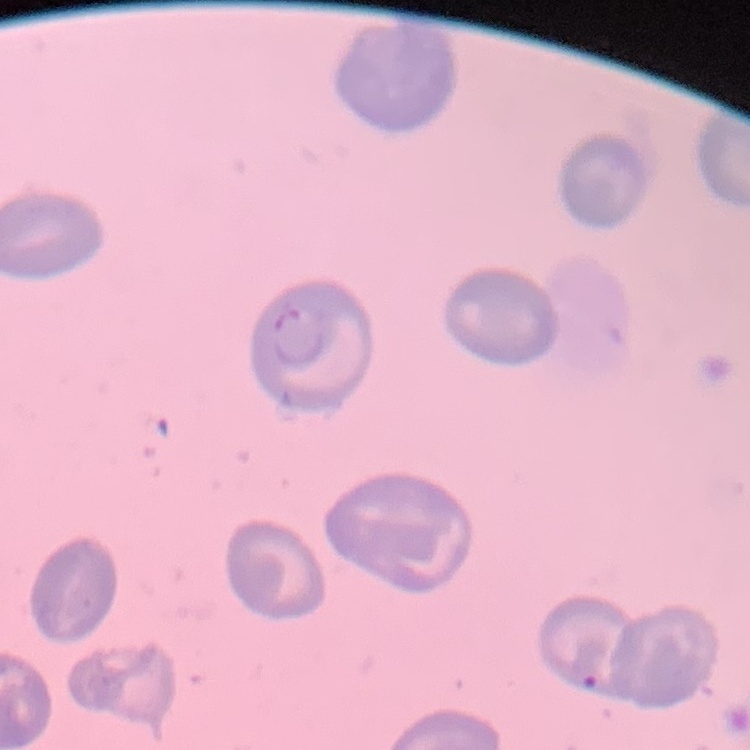
Summary:
  - Red blood cell morphology: no rouleaux formation
  - Stain: Field's or Giemsa
  - Preparation: thin blood smear
  - Image type: square crop of a larger photomicrograph